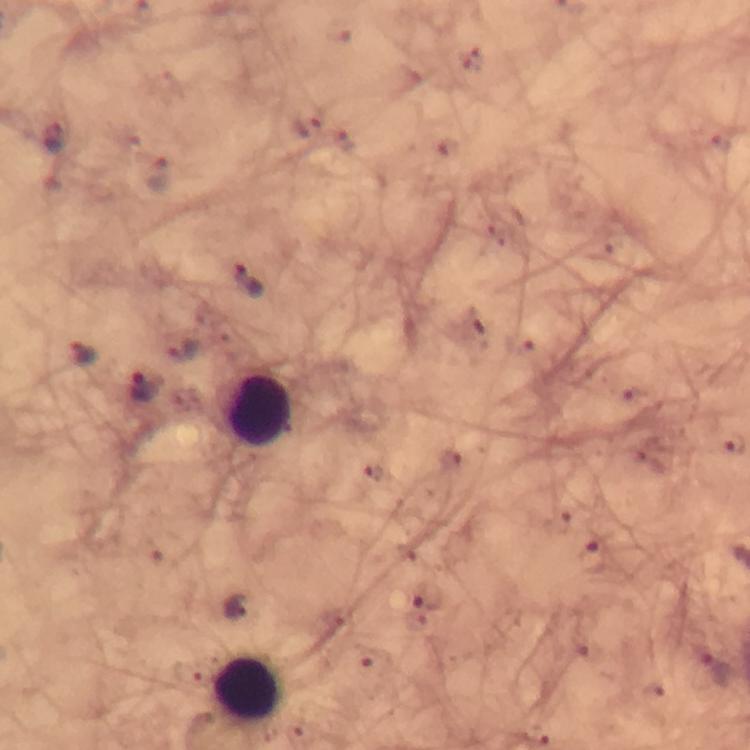

Approximate centers as {x, y} in pixels.
Summary:
  - Leukocyte locations: {259, 408}, {245, 687}
  - Plasmodium parasite locations: {304, 126}, {55, 137}, {345, 143}, {157, 174}, {248, 278}, {184, 349}, {83, 350}, {144, 385}, {591, 557}, {428, 596}, {236, 606}, {372, 657}, {714, 669}
  - Preparation: thick blood smear
  - Cropped from: a single field of view
  - Context: from a diagnostic examination for malaria
  - Capture: smartphone photograph through a microscope
  - Stain: Giemsa
  - Image size: 750×750 pixels
  - Magnification: 100x
  - Immersion oil: used